Name the parasite shown.
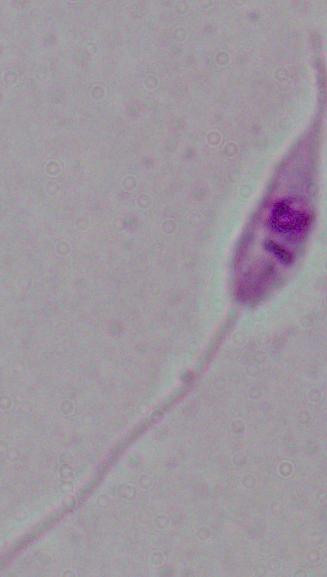

Leishmania.

Summary:
  - Magnification: 1000x
  - Modality: micrograph